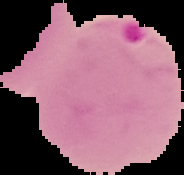

{
  "result": "Plasmodium parasites identified",
  "image_type": "cell region segmented out of the field of view; surrounding area masked to black",
  "preparation": "thin blood film",
  "image_size": "184×175 pixels"
}